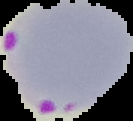

Segmented cell region on a black background. Result: malaria parasites detected. From a thin blood smear. Image is 133×121 pixels.